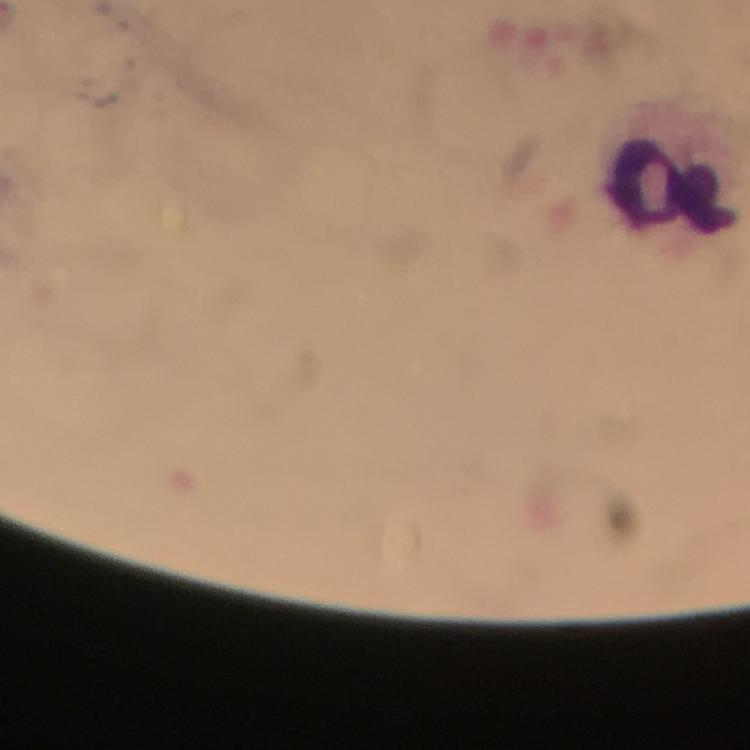
stain = Giemsa
magnification = 100x
malaria parasites = none detected
capture = smartphone mounted on the microscope
immersion oil = applied
context = from a malaria diagnostic workup
cropped from = one field of view
leukocyte locations = approximate centers as [x, y] in pixels: [669, 185]
preparation = thick blood smear
image size = 750×750 pixels